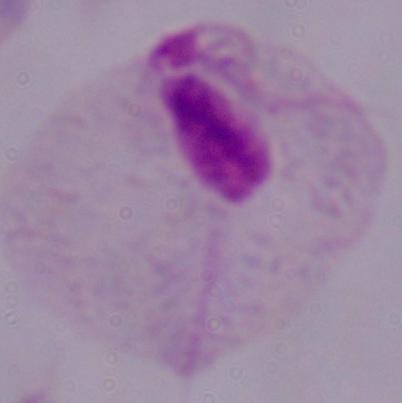
{
  "modality": "photomicrograph",
  "identification": "trichomonad",
  "magnification": "1000x"
}